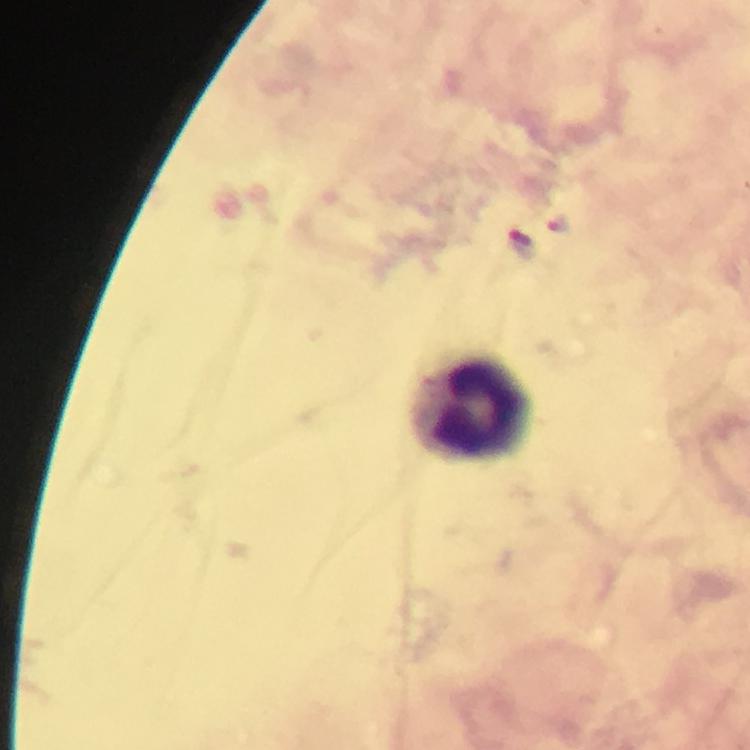

Approximate centers as [x, y] in pixels.
Summary:
  - Malaria parasite locations: [521, 246]
  - Leukocyte locations: [473, 408]
  - Stain: Giemsa
  - Immersion oil: applied
  - Preparation: thick blood film
  - Image size: 750×750 pixels
  - Capture: smartphone photograph through a microscope
  - Cropped from: a single field of view
  - Magnification: 100x
  - Context: from a malaria diagnostic workup